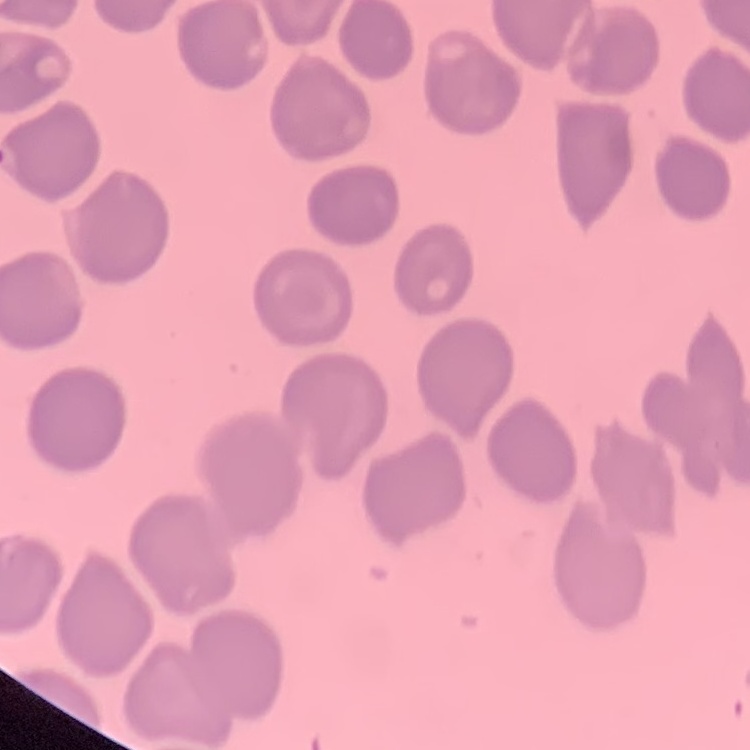

The red blood cells show no rouleaux formation. Field's or Giemsa stain. One tile cut from a larger photomicrograph. Thin peripheral smear.